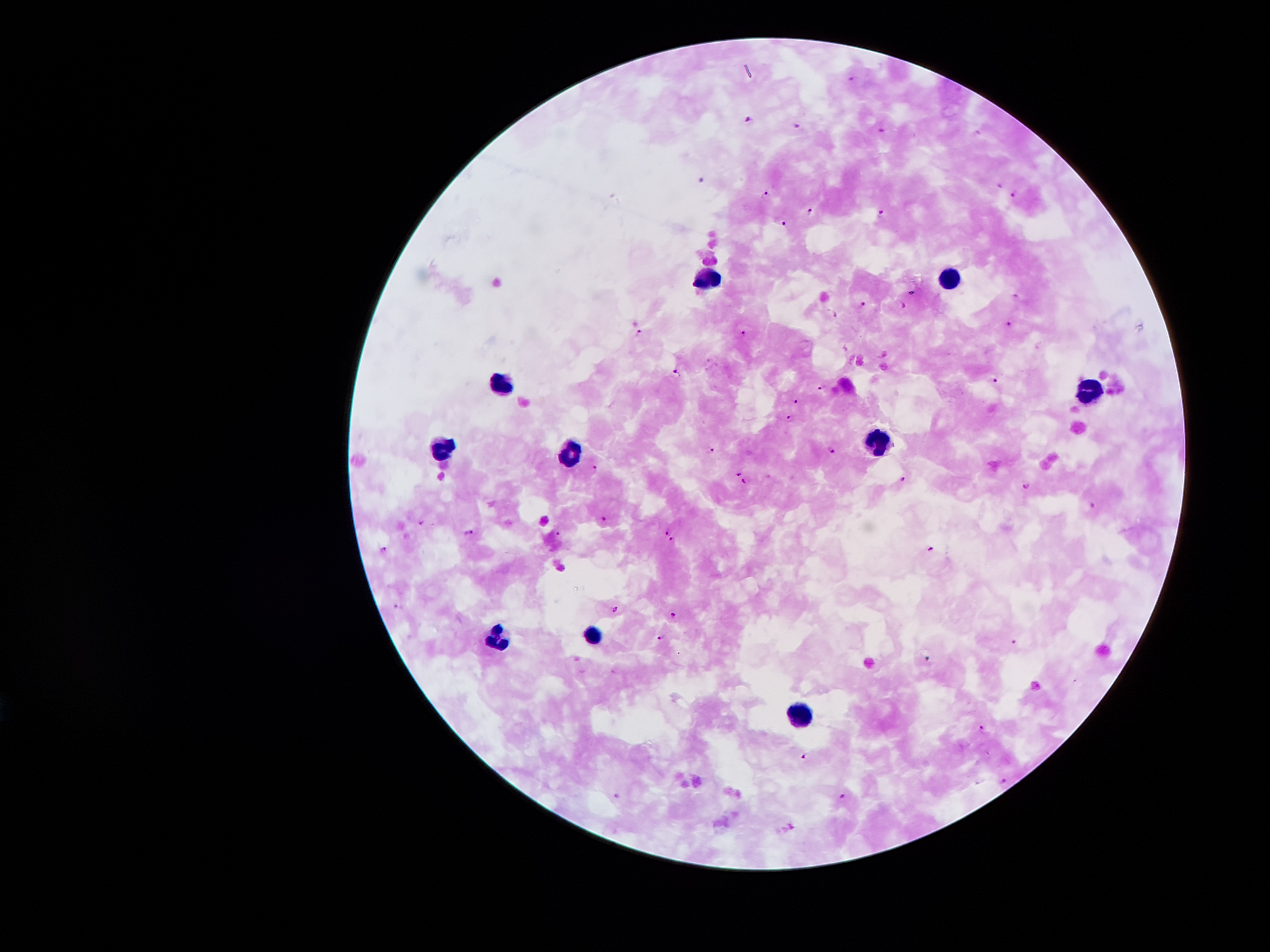

Approximate object centers, in pixels from the top-left corner.
Summary:
  - Plasmodium parasite locations: (x=852, y=79), (x=748, y=120), (x=798, y=127), (x=881, y=133), (x=1001, y=183), (x=767, y=195), (x=1014, y=195), (x=810, y=211), (x=881, y=214), (x=783, y=222), (x=1015, y=295), (x=865, y=303), (x=903, y=304), (x=836, y=314), (x=1010, y=324), (x=639, y=333), (x=743, y=333), (x=678, y=373), (x=994, y=381), (x=820, y=389), (x=795, y=401), (x=787, y=417), (x=712, y=451), (x=831, y=451), (x=595, y=466), (x=739, y=472), (x=904, y=480), (x=746, y=481), (x=1027, y=485), (x=1092, y=506), (x=603, y=519), (x=422, y=523), (x=666, y=530), (x=469, y=533), (x=558, y=533), (x=673, y=539), (x=932, y=549), (x=385, y=550), (x=395, y=605), (x=614, y=608), (x=674, y=614), (x=661, y=638), (x=1015, y=641), (x=983, y=726), (x=805, y=756), (x=1004, y=780), (x=843, y=795), (x=617, y=796)
  - Leukocyte locations: (x=701, y=275), (x=951, y=281), (x=502, y=383), (x=1092, y=387), (x=881, y=439), (x=444, y=446), (x=571, y=456), (x=593, y=634), (x=497, y=641), (x=801, y=713)
  - Field of view: single
  - Magnification: 100x
  - Capture: smartphone through the microscope eyepiece
  - Preparation: thick blood smear
  - Stain: Giemsa
  - Image size: 1270×952 pixels
  - Patient malaria status: infected with Plasmodium falciparum